Report the malaria status of this cell.
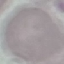
Uninfected.

Acquired by smartphone through the microscope eyepiece. Thin blood smear. Cell patch, automatically extracted from a larger field of view and resized to 64 × 64 pixels. Giemsa-stained preparation.